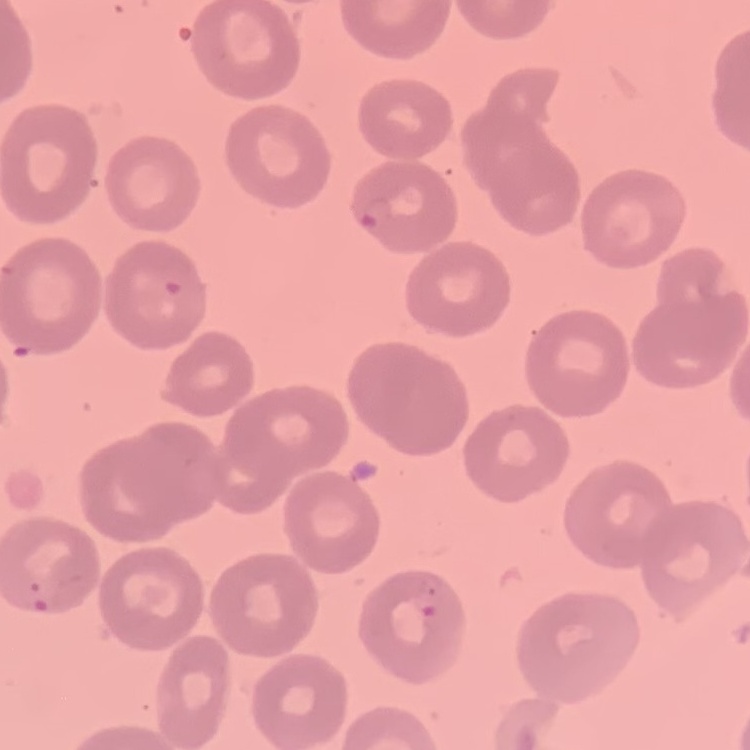

erythrocyte morphology = no rouleaux formation
preparation = thin blood smear
stain = Field's or Giemsa
image type = square crop of a larger photomicrograph